Name the cell type shown.
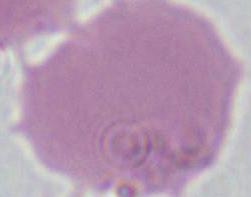
This is an erythrocyte.

Summary:
  - Modality: micrograph
  - Magnification: 1000x